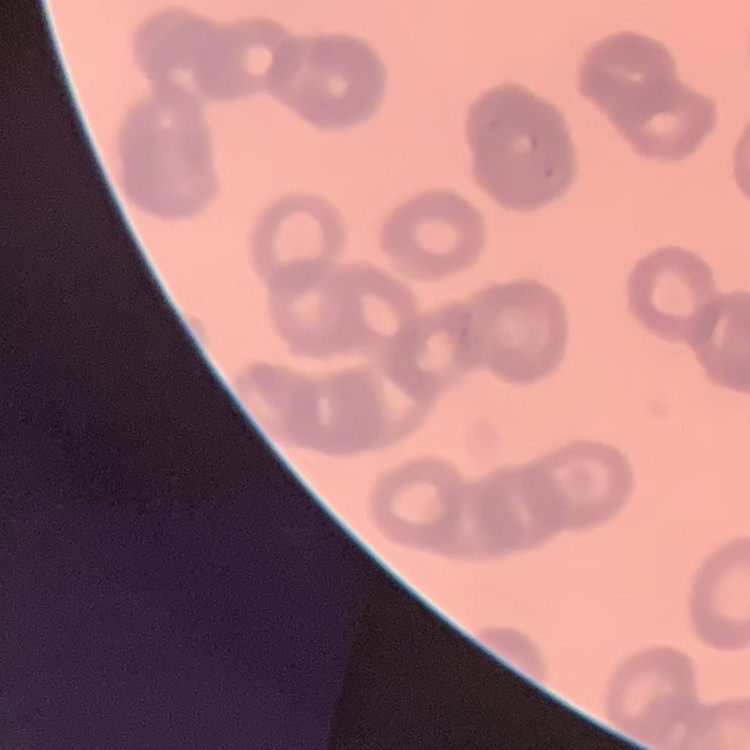
red blood cell morphology = rouleaux formation
stain = Field's or Giemsa
preparation = thin blood film
image type = one tile cut from a larger photomicrograph